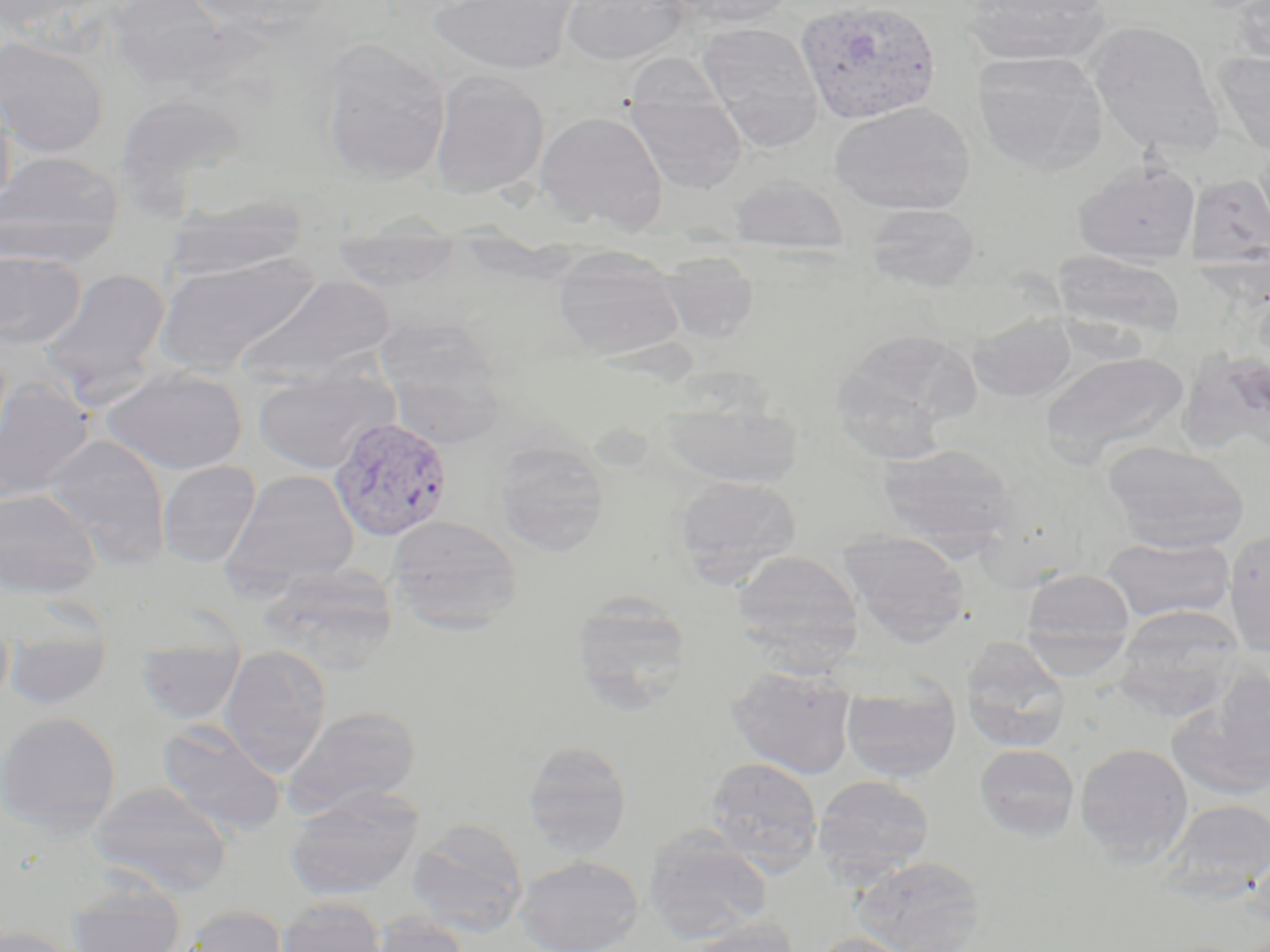

Approximate bounding boxes as (x1, y1, x2, y2) in pixels. Plasmodium vivax-infected red blood cell locations: (795, 0, 942, 125), (328, 417, 454, 542). Uninfected red blood cell locations: (0, 0, 100, 35), (108, 0, 228, 91), (186, 0, 339, 39), (428, 0, 579, 75), (560, 0, 690, 65), (667, 0, 797, 29), (960, 0, 1113, 67), (1230, 0, 1270, 73), (1086, 21, 1222, 156), (696, 22, 824, 148), (0, 37, 108, 157), (319, 37, 451, 185), (972, 51, 1109, 175), (1215, 51, 1270, 158), (624, 53, 728, 113), (429, 70, 550, 198), (0, 89, 16, 216), (114, 91, 248, 213), (625, 92, 746, 196), (829, 102, 976, 215), (535, 111, 668, 232), (0, 151, 123, 266), (1072, 158, 1201, 265), (729, 174, 849, 253), (1186, 174, 1270, 268), (164, 194, 309, 282), (864, 204, 982, 293), (329, 231, 464, 292), (552, 246, 686, 362), (0, 249, 86, 350), (1053, 250, 1186, 340), (153, 251, 322, 376), (659, 252, 760, 344), (39, 267, 172, 402), (238, 275, 396, 386), (967, 311, 1077, 402), (373, 314, 506, 434), (838, 328, 980, 434), (1178, 347, 1270, 462), (1038, 351, 1190, 467), (102, 365, 249, 475), (253, 365, 398, 473), (0, 377, 94, 503), (661, 397, 802, 490), (42, 432, 172, 566), (491, 437, 611, 557), (1103, 440, 1251, 553), (876, 443, 1018, 553), (157, 460, 261, 567), (221, 469, 361, 593), (672, 475, 803, 585), (0, 487, 101, 599), (386, 515, 523, 632), (1224, 529, 1270, 656), (839, 530, 971, 645), (1101, 537, 1236, 623), (731, 549, 864, 662), (259, 565, 399, 671), (1019, 568, 1136, 664), (570, 594, 694, 709), (1112, 605, 1247, 717), (960, 638, 1071, 752), (0, 643, 14, 710), (3, 643, 114, 709), (219, 644, 331, 774), (136, 653, 245, 723), (725, 665, 857, 779), (1167, 672, 1270, 803), (840, 680, 961, 781), (283, 704, 422, 819), (0, 711, 121, 833), (158, 719, 287, 838), (522, 739, 633, 858), (1074, 742, 1194, 864), (974, 743, 1080, 842), (704, 756, 823, 871), (813, 774, 935, 882), (90, 781, 233, 897), (283, 787, 424, 901), (1156, 798, 1270, 902), (407, 818, 529, 937), (642, 826, 774, 941), (515, 854, 644, 952), (852, 854, 985, 952), (65, 884, 188, 952), (276, 897, 387, 952), (178, 904, 289, 952), (366, 912, 472, 952), (685, 917, 797, 952), (0, 924, 83, 952), (808, 932, 915, 952). Slide-level diagnosis: Plasmodium vivax. Image is 1270×952 pixels. Light microscopy. One field of a larger specimen. Thin blood film. 1000x magnification. May-Grünwald-Giemsa stain.